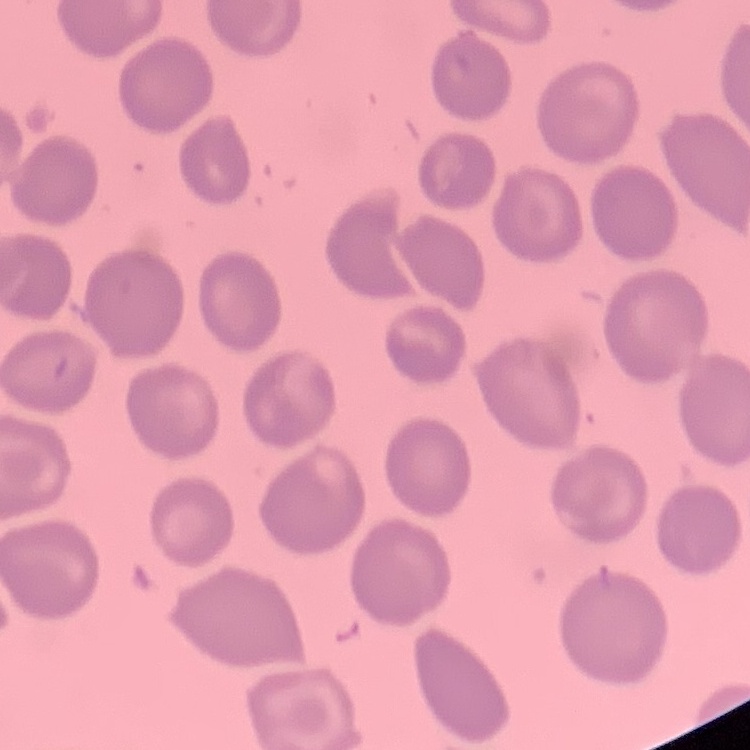
Summary:
  - Erythrocyte morphology: no rouleaux formation
  - Stain: Field's or Giemsa
  - Image type: one tile cut from a larger photomicrograph
  - Preparation: thin blood film